Comment on the morphology of the erythrocytes.
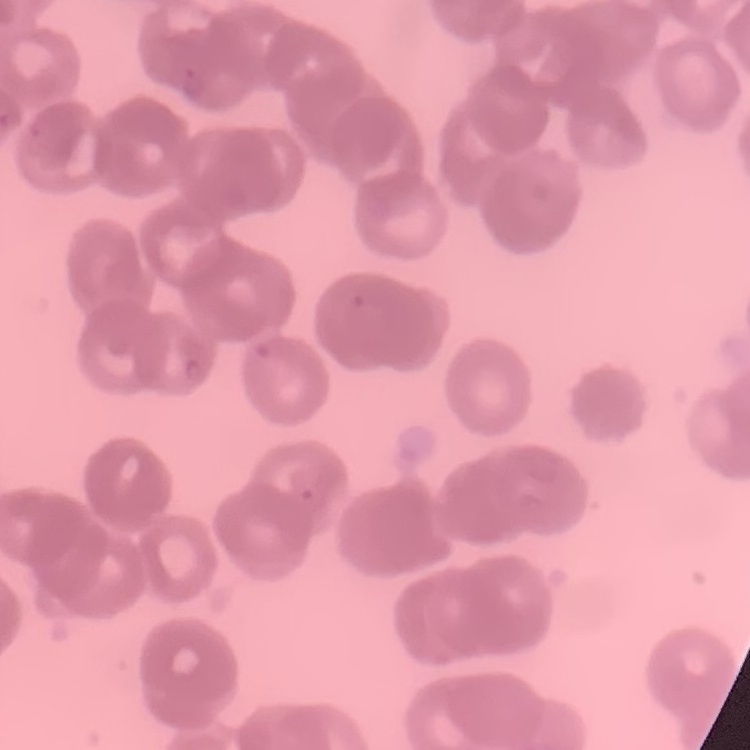
Rouleaux formation.

Field's or Giemsa stain. Thin blood film. One tile cut from a larger photomicrograph.